Assess this cell for malaria.
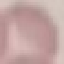

It is uninfected.

image type = automatically extracted cell patch, resized to 64 × 64 pixels
preparation = thin blood smear
stain = Giemsa
capture = smartphone through the microscope eyepiece